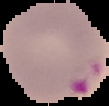

preparation = thin blood film
malaria status = parasitized
image size = 109×106 pixels
image type = cell region segmented out of the field of view; surrounding area masked to black